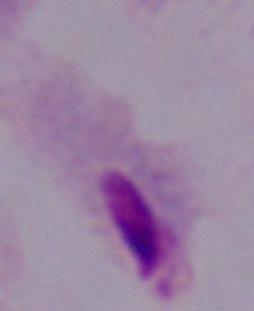
Captured at 1000x magnification. Micrograph. A trichomonad is seen.